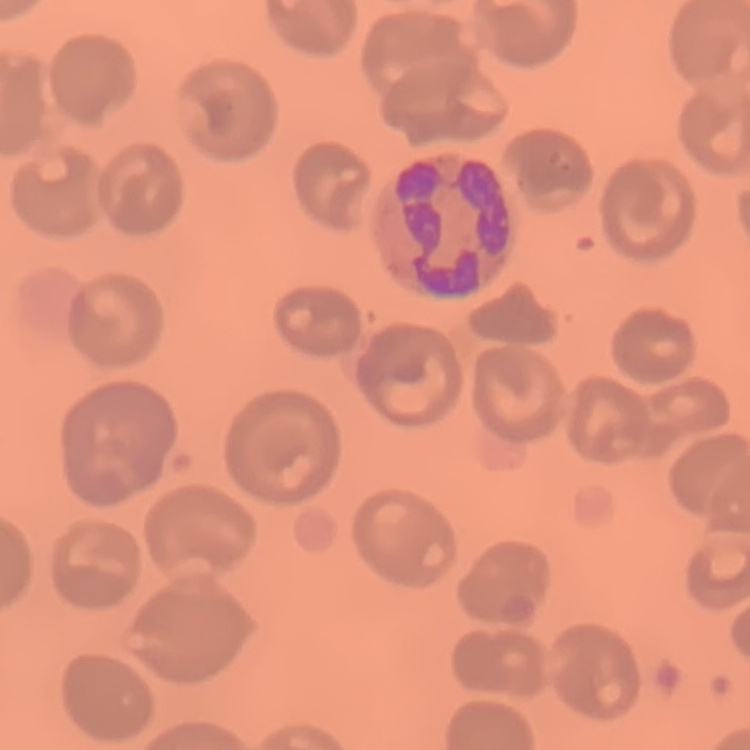
Summary:
  - Erythrocyte morphology: no rouleaux formation
  - Stain: Field's or Giemsa
  - Preparation: thin peripheral smear
  - Image type: square crop of a larger photomicrograph